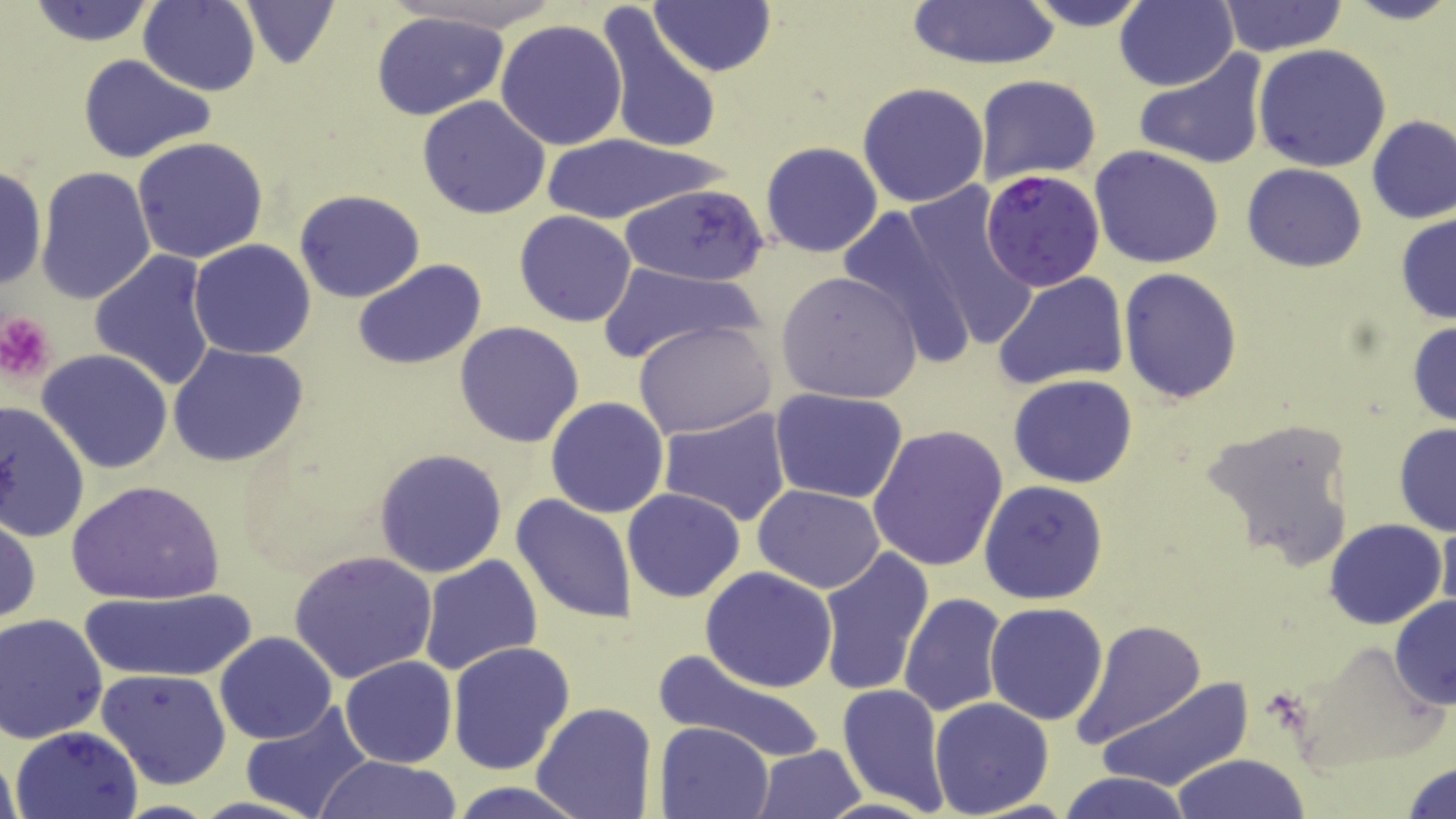

Summary:
  - Coordinate format: approximate bounding boxes as named x1/y1/x2/y2 corners in pixels
  - Platelet locations: (x1=0, y1=311, x2=57, y2=383)
  - Plasmodium falciparum-infected red blood cell locations: (x1=980, y1=171, x2=1106, y2=291)
  - Uninfected red blood cell locations: (x1=23, y1=0, x2=161, y2=47), (x1=239, y1=0, x2=341, y2=70), (x1=389, y1=0, x2=569, y2=34), (x1=650, y1=0, x2=776, y2=76), (x1=905, y1=0, x2=1061, y2=71), (x1=1018, y1=0, x2=1157, y2=30), (x1=1115, y1=0, x2=1238, y2=92), (x1=1338, y1=0, x2=1456, y2=26), (x1=137, y1=1, x2=261, y2=94), (x1=1218, y1=1, x2=1348, y2=57), (x1=595, y1=6, x2=721, y2=157), (x1=370, y1=10, x2=510, y2=121), (x1=495, y1=19, x2=628, y2=151), (x1=1254, y1=44, x2=1391, y2=173), (x1=1134, y1=50, x2=1270, y2=171), (x1=77, y1=53, x2=218, y2=165), (x1=974, y1=74, x2=1102, y2=188), (x1=858, y1=81, x2=989, y2=208), (x1=417, y1=95, x2=551, y2=220), (x1=1365, y1=115, x2=1456, y2=225), (x1=536, y1=133, x2=722, y2=223), (x1=133, y1=136, x2=269, y2=263), (x1=760, y1=141, x2=884, y2=258), (x1=1090, y1=146, x2=1224, y2=267), (x1=1241, y1=163, x2=1366, y2=272), (x1=0, y1=165, x2=48, y2=292), (x1=35, y1=165, x2=158, y2=306), (x1=620, y1=181, x2=771, y2=287), (x1=293, y1=189, x2=426, y2=303), (x1=900, y1=190, x2=1041, y2=355), (x1=835, y1=205, x2=981, y2=366), (x1=515, y1=211, x2=637, y2=327), (x1=1394, y1=212, x2=1456, y2=326), (x1=187, y1=239, x2=316, y2=360), (x1=88, y1=250, x2=219, y2=392), (x1=353, y1=258, x2=487, y2=371), (x1=597, y1=262, x2=763, y2=366), (x1=1118, y1=269, x2=1242, y2=403), (x1=776, y1=271, x2=923, y2=405), (x1=993, y1=271, x2=1130, y2=390), (x1=633, y1=320, x2=778, y2=439), (x1=1407, y1=320, x2=1456, y2=428), (x1=454, y1=321, x2=585, y2=447), (x1=167, y1=342, x2=309, y2=467), (x1=37, y1=349, x2=174, y2=475), (x1=1009, y1=374, x2=1138, y2=489), (x1=767, y1=387, x2=909, y2=505), (x1=545, y1=396, x2=668, y2=518), (x1=0, y1=399, x2=91, y2=545), (x1=658, y1=407, x2=793, y2=527), (x1=1198, y1=413, x2=1358, y2=571), (x1=1393, y1=423, x2=1456, y2=536), (x1=867, y1=424, x2=1008, y2=572), (x1=372, y1=447, x2=508, y2=579), (x1=65, y1=479, x2=225, y2=605), (x1=979, y1=480, x2=1109, y2=603), (x1=754, y1=484, x2=885, y2=594), (x1=621, y1=488, x2=746, y2=603), (x1=511, y1=493, x2=638, y2=626), (x1=0, y1=511, x2=41, y2=631), (x1=1438, y1=515, x2=1456, y2=621), (x1=1324, y1=519, x2=1446, y2=631), (x1=816, y1=548, x2=936, y2=696), (x1=289, y1=550, x2=440, y2=686), (x1=418, y1=554, x2=541, y2=675), (x1=699, y1=566, x2=839, y2=692), (x1=77, y1=589, x2=255, y2=681), (x1=899, y1=594, x2=1005, y2=717), (x1=1389, y1=595, x2=1456, y2=710), (x1=984, y1=601, x2=1109, y2=724), (x1=1, y1=613, x2=108, y2=743), (x1=1070, y1=617, x2=1208, y2=749), (x1=215, y1=631, x2=338, y2=744), (x1=446, y1=641, x2=576, y2=777), (x1=646, y1=648, x2=830, y2=767), (x1=338, y1=657, x2=456, y2=768), (x1=95, y1=669, x2=231, y2=789), (x1=1096, y1=677, x2=1253, y2=794), (x1=837, y1=683, x2=950, y2=816), (x1=929, y1=698, x2=1054, y2=818), (x1=530, y1=701, x2=657, y2=819), (x1=240, y1=703, x2=374, y2=819), (x1=656, y1=721, x2=773, y2=818), (x1=9, y1=726, x2=143, y2=819), (x1=752, y1=744, x2=868, y2=819), (x1=1171, y1=752, x2=1310, y2=819), (x1=313, y1=756, x2=467, y2=818), (x1=1402, y1=759, x2=1456, y2=818), (x1=1056, y1=771, x2=1194, y2=819), (x1=446, y1=782, x2=592, y2=818)
  - Slide-level diagnosis: Plasmodium falciparum
  - Preparation: thin blood smear
  - Modality: optical microscopy
  - Stain: May-Grünwald-Giemsa
  - Magnification: 1000x
  - Field of view: one of a larger specimen
  - Image size: 1456×819 pixels